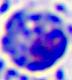 A white blood cell is shown. Captured at 400x magnification. Micrograph.